Describe the morphology of the red blood cells.
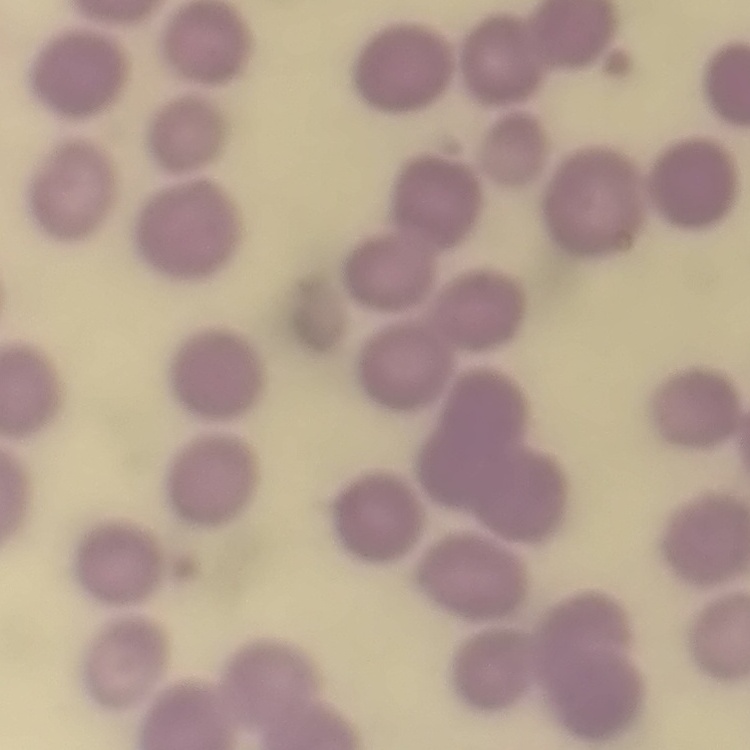

They show no rouleaux formation.

Stained with either Field's or Giemsa. One tile cut from a larger photomicrograph. Thin peripheral smear.